Identify the preparation type.
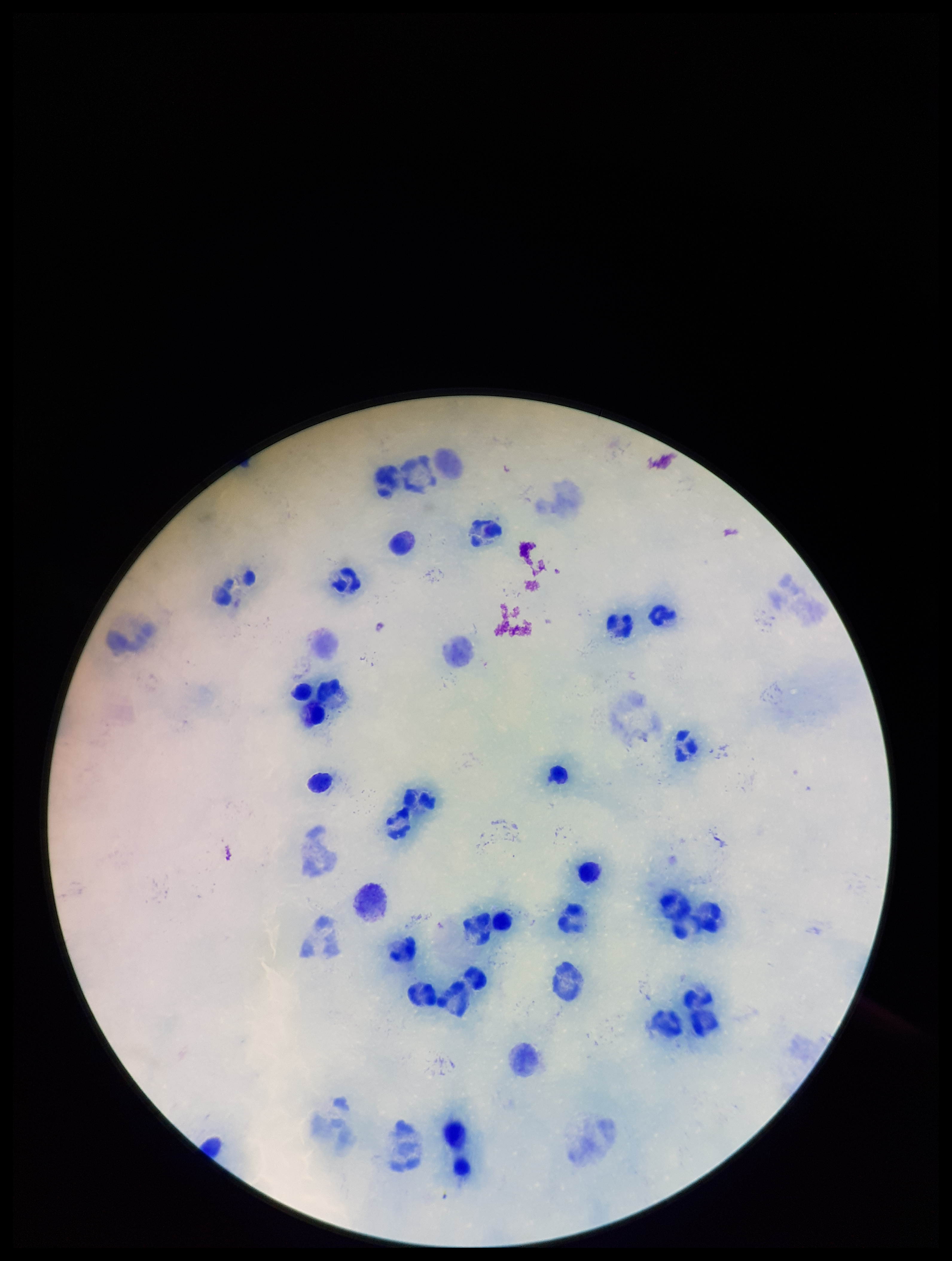
A thick smear.

Leukocyte count: 28. Giemsa stain. Patient malaria status: negative. Parasite count: 0. Image is 952×1261 pixels. One field from this slide. Smartphone photograph taken through the eyepiece of a microscope. Plasmodium parasites: none seen.